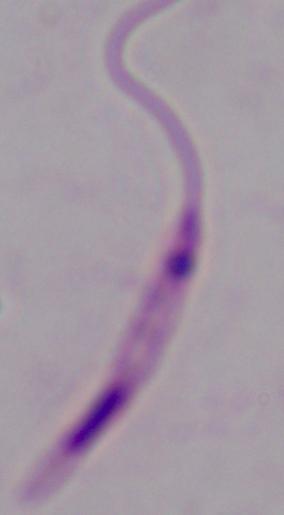

modality = micrograph
magnification = 1000x
identification = Leishmania